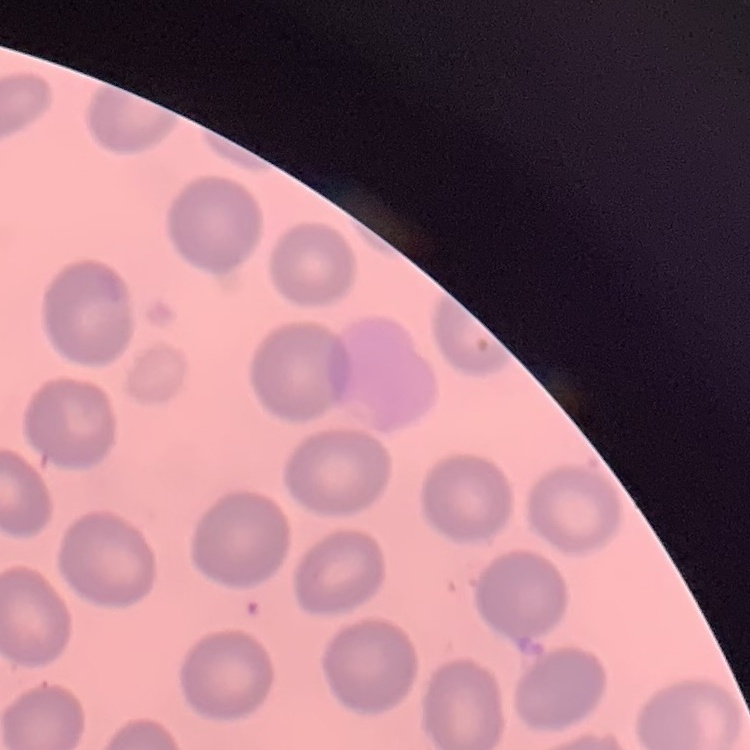
erythrocyte morphology = no rouleaux formation
preparation = thin blood smear
stain = Field's or Giemsa
image type = square crop of a larger photomicrograph